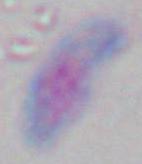

Summary:
  - Magnification: 1000x
  - Identification: Toxoplasma gondii
  - Modality: photomicrograph